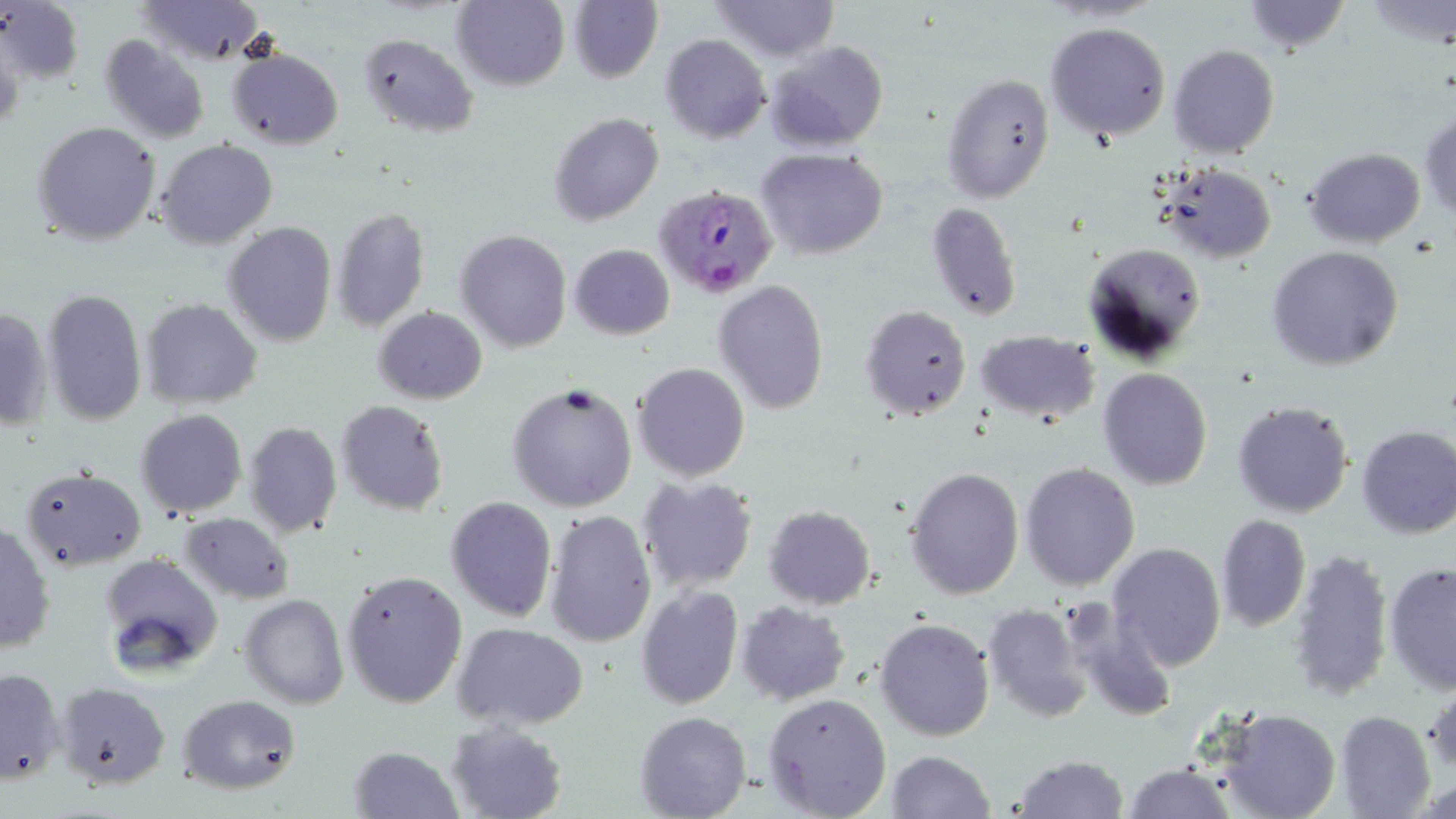

slide-level diagnosis = Plasmodium falciparum
preparation = thin blood smear
uninfected red blood cell locations = approximate bounding boxes as (x1, y1, x2, y2) in pixels: (137, 0, 266, 64), (454, 0, 569, 89), (567, 0, 662, 83), (710, 0, 840, 63), (1238, 0, 1352, 55), (0, 1, 86, 85), (1046, 22, 1171, 140), (359, 34, 479, 135), (660, 34, 770, 144), (98, 35, 210, 144), (763, 40, 888, 150), (1169, 44, 1280, 160), (226, 46, 343, 150), (942, 71, 1055, 203), (1419, 108, 1456, 224), (549, 112, 663, 225), (33, 122, 161, 246), (155, 138, 278, 249), (756, 146, 888, 260), (1304, 147, 1426, 247), (1158, 162, 1277, 261), (926, 203, 1023, 322), (331, 209, 430, 330), (224, 222, 337, 348), (454, 229, 573, 352), (1085, 241, 1208, 361), (569, 244, 675, 339), (1266, 245, 1404, 370), (712, 280, 830, 414), (42, 289, 148, 425), (141, 298, 262, 411), (858, 304, 972, 421), (0, 306, 51, 431), (374, 306, 487, 404), (974, 329, 1099, 422), (632, 362, 749, 482), (1098, 368, 1213, 491), (506, 381, 639, 513), (1231, 399, 1355, 519), (335, 400, 449, 516), (135, 409, 246, 518), (243, 420, 343, 539), (1355, 425, 1456, 539), (1019, 462, 1140, 591), (903, 465, 1026, 601), (20, 469, 146, 570), (638, 477, 757, 592), (444, 496, 558, 623), (762, 504, 875, 609), (544, 509, 657, 649), (179, 511, 295, 603), (1215, 514, 1310, 633), (1, 523, 54, 654), (1108, 542, 1228, 671), (1288, 546, 1394, 703), (98, 552, 223, 678), (1382, 562, 1454, 694), (342, 570, 469, 709), (635, 586, 744, 710), (242, 593, 348, 709), (735, 602, 850, 705), (981, 603, 1095, 723), (875, 617, 994, 740), (454, 623, 589, 730), (1, 667, 66, 785), (1426, 680, 1456, 783), (58, 683, 170, 788), (180, 693, 301, 795), (763, 693, 892, 819), (1217, 707, 1342, 819), (1334, 710, 1436, 819), (635, 711, 751, 819), (444, 719, 569, 819), (348, 745, 465, 818), (885, 750, 994, 819), (1010, 755, 1129, 818), (1121, 762, 1236, 819)
field of view = one of a larger specimen
modality = light microscopy
image size = 1456×819 pixels
stain = May-Grünwald-Giemsa
magnification = 1000x
Plasmodium falciparum-infected red blood cell locations = approximate bounding boxes as (x1, y1, x2, y2) in pixels: (649, 182, 775, 296)